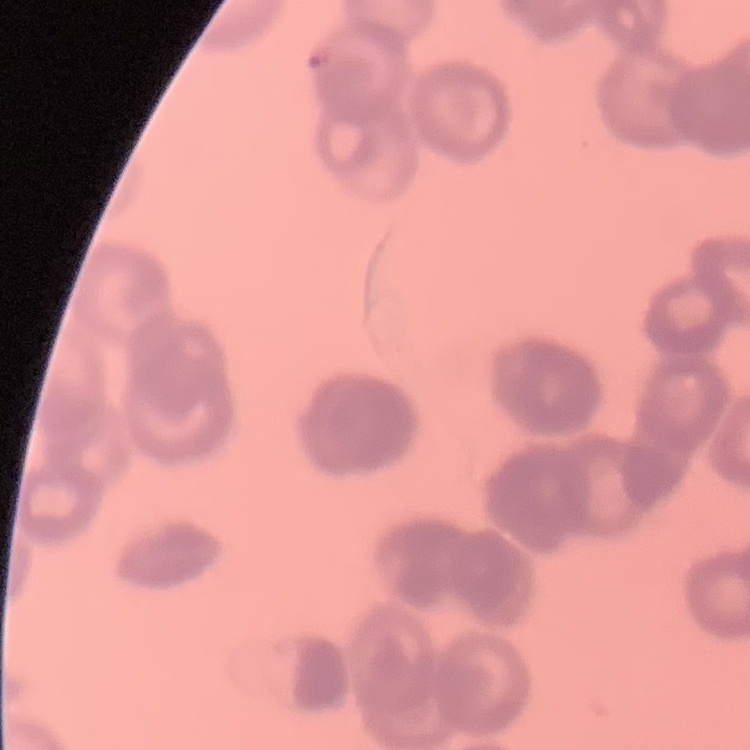

red blood cell morphology = rouleaux formation
stain = Field's or Giemsa
preparation = thin blood smear
image type = square crop of a larger photomicrograph